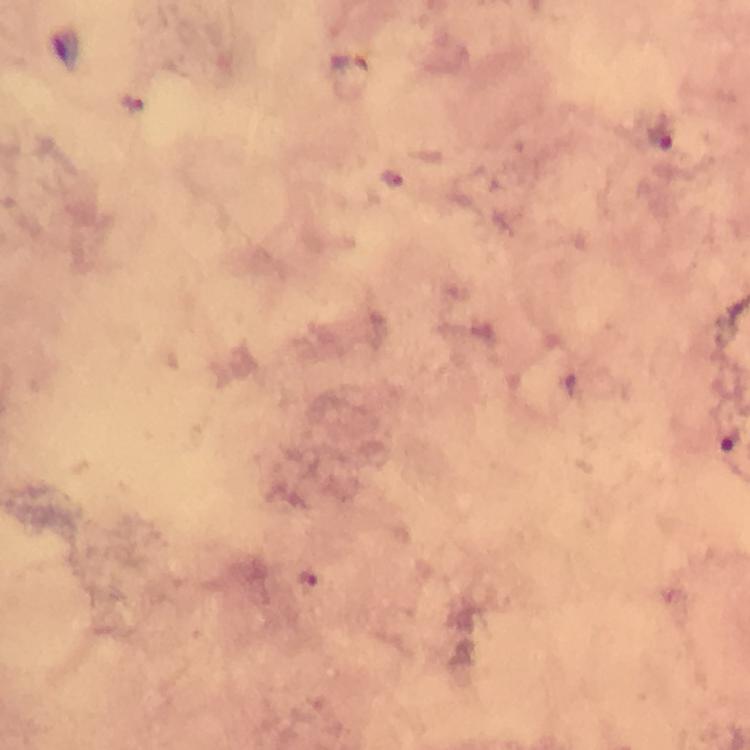

Approximate centers as {x, y} in pixels. Malaria parasite locations: {662, 137}, {394, 178}, {728, 444}, {309, 577}. Immersion oil applied. Cropped region of a single field of view. At 100x magnification. Image is 750×750 pixels. Thick blood film. From a diagnostic examination for malaria. Photographed through the microscope with a smartphone camera. Giemsa stain.